Assess this cell for malaria.
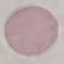

It is uninfected.

Thin smear of blood. Giemsa stain. Cell patch, automatically extracted from a larger field of view and resized to 64 × 64 pixels. Acquired by smartphone through the microscope eyepiece.